Report the malaria status of this cell.
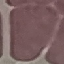

Uninfected.

Automatically extracted cell patch, resized to 64 × 64 pixels. Giemsa stain. Thin blood film. Photographed with a smartphone camera at the microscope eyepiece.